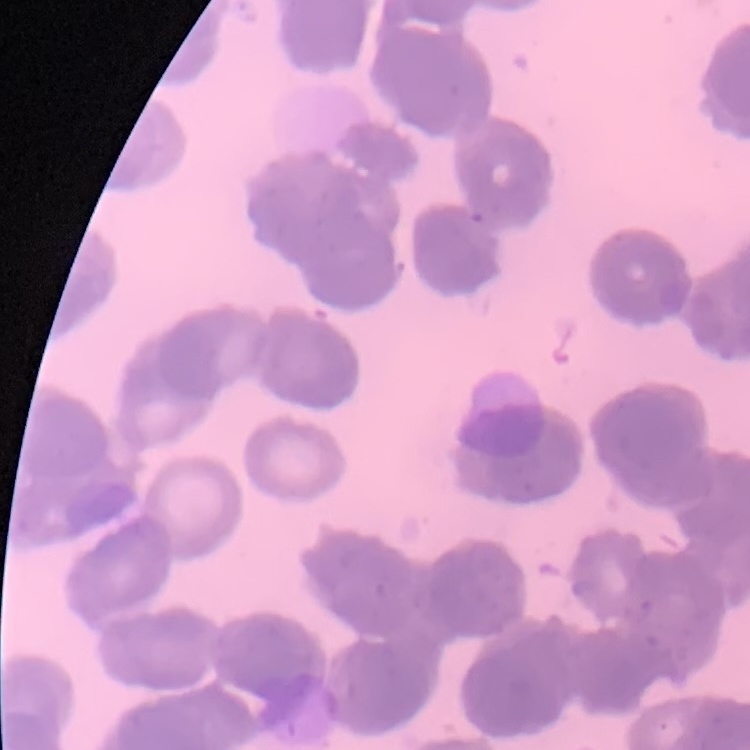
Summary:
  - Erythrocyte morphology: rouleaux formation
  - Image type: one tile cut from a larger photomicrograph
  - Stain: Field's or Giemsa
  - Preparation: thin blood film